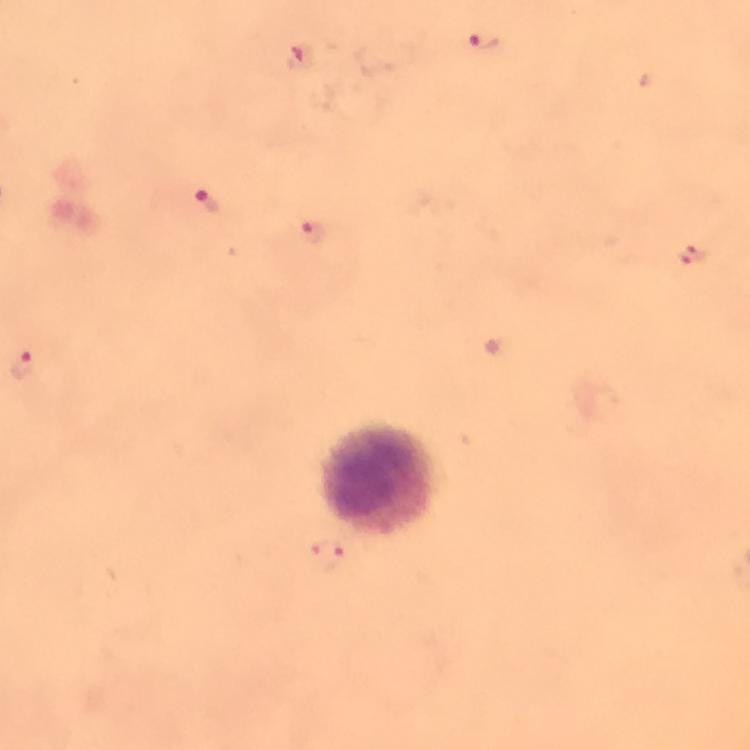

Approximate centers as {x, y} in pixels.
Summary:
  - Leukocyte locations: {382, 477}
  - Malaria parasite locations: {482, 41}, {300, 59}, {206, 202}, {312, 229}, {693, 253}, {24, 365}
  - Immersion oil: applied
  - Context: from a diagnostic examination for malaria
  - Preparation: thick blood smear
  - Magnification: 100x
  - Image size: 750×750 pixels
  - Stain: Giemsa
  - Cropped from: one field of view
  - Capture: smartphone photograph through a microscope